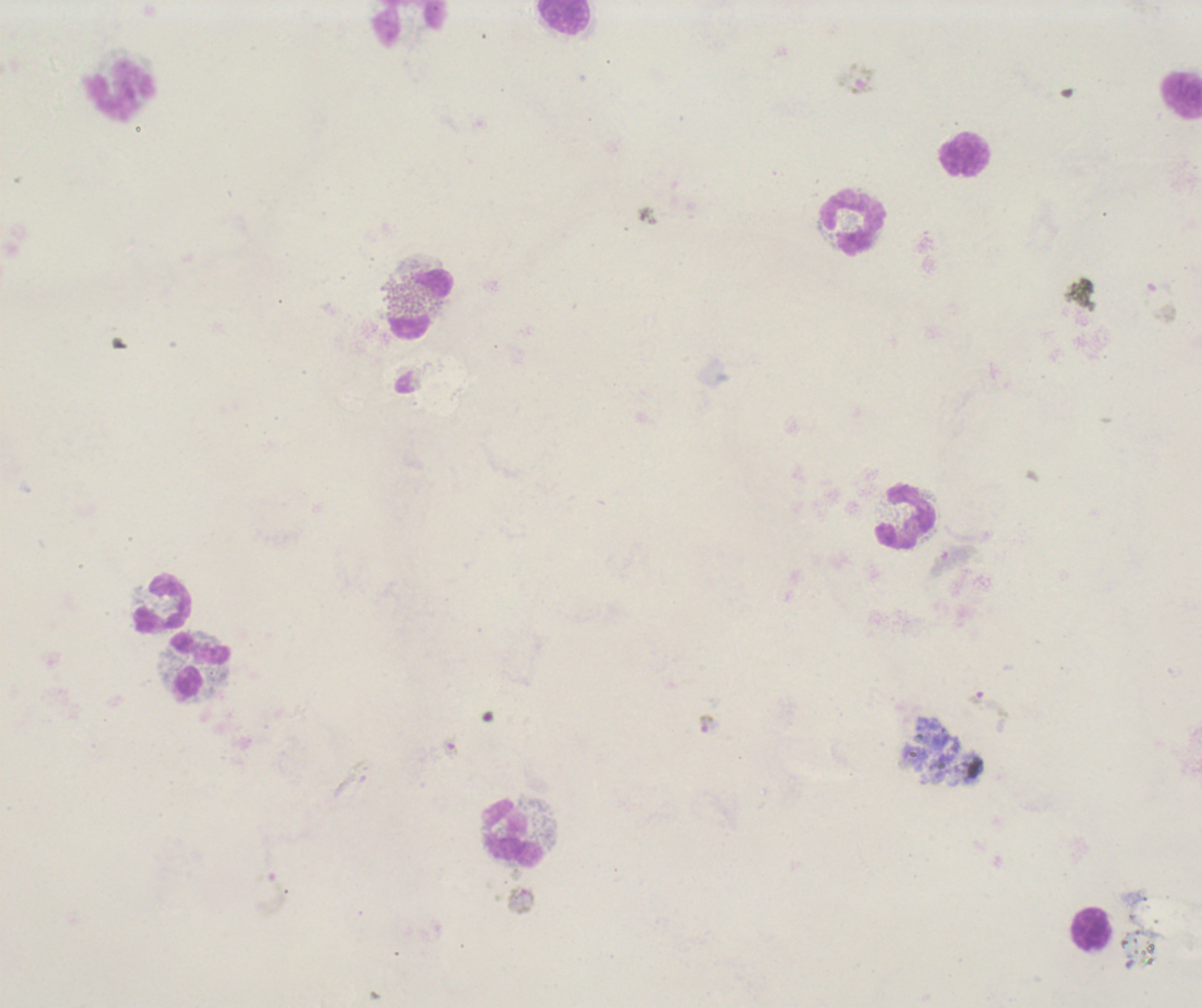
Approximate centers as {x, y} in pixels.
Summary:
  - Trophozoite locations: {707, 725}
  - Leukocyte locations: {563, 17}, {410, 24}, {121, 91}, {1180, 95}, {964, 154}, {853, 222}, {420, 304}, {905, 515}, {162, 603}, {200, 664}, {514, 834}, {1092, 929}
  - Gametocyte locations: {857, 78}, {1160, 300}, {953, 561}, {990, 703}, {451, 747}, {350, 778}
  - Life-cycle stages observed: trophozoite, gametocyte
  - Context: previously used in a real diagnosis
  - Result: positive for malaria parasites
  - Magnification: 100x
  - Field of view: one from this slide
  - Preparation: thick blood smear
  - Coloration quality: bad
  - Image size: 1202×1008 pixels
  - Background quality: poor
  - Stain: Romanowsky